Classify this cell by malaria status.
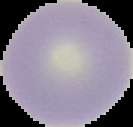

It is uninfected.

Summary:
  - Preparation: thin blood smear
  - Image size: 133×127 pixels
  - Image type: cell region segmented out of the field of view; surrounding area masked to black